State the preparation type.
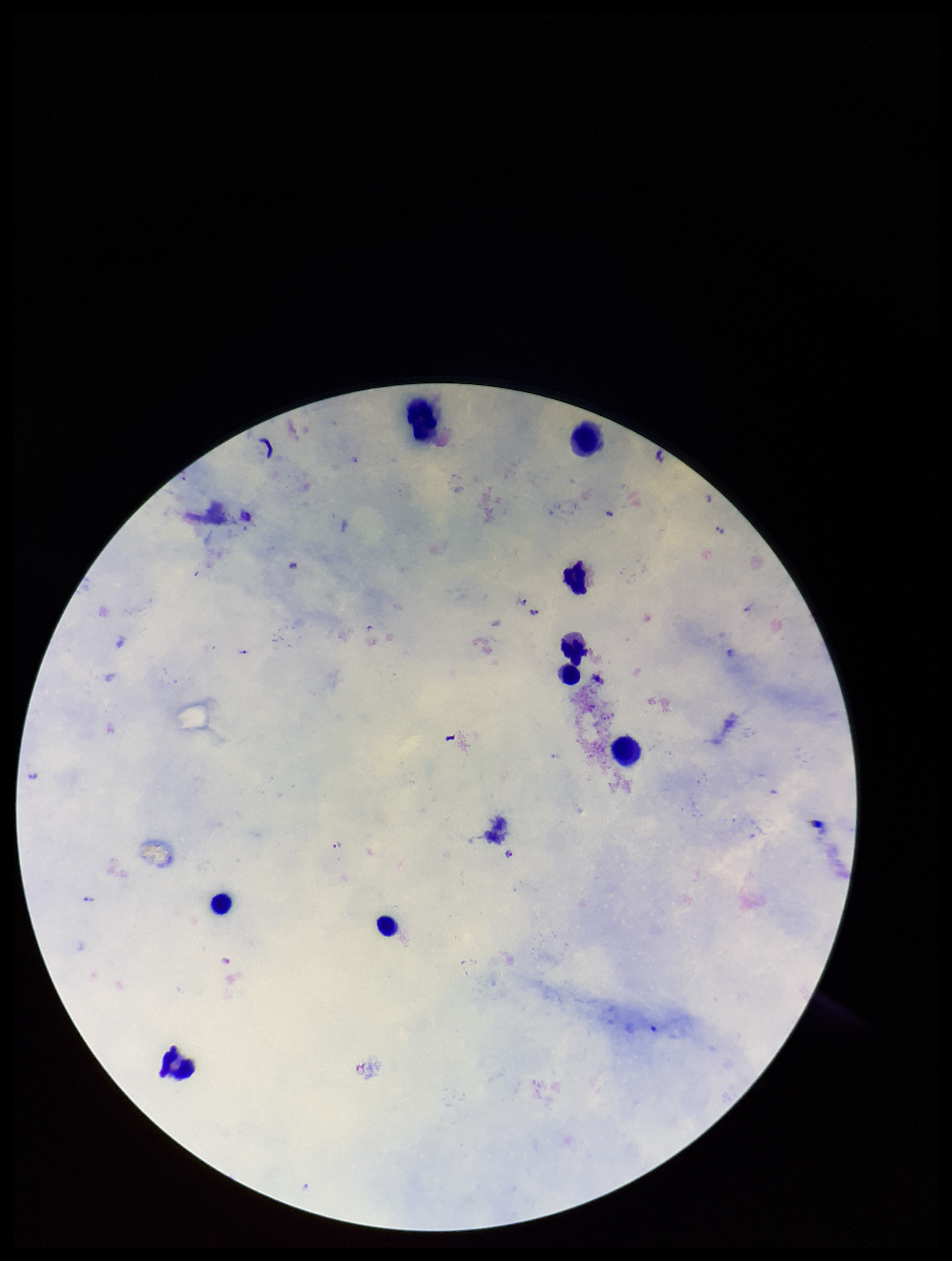

It is a thick blood smear.

Patient malaria status: infected. Image is 952×1261 pixels. Parasite count: 9. Leukocyte count: 9. Species reported for this patient: Plasmodium falciparum. Plasmodium parasites: detected. Single field of view. Giemsa stain. Photographed through the microscope eyepiece with a smartphone camera.